State the blood parasite species.
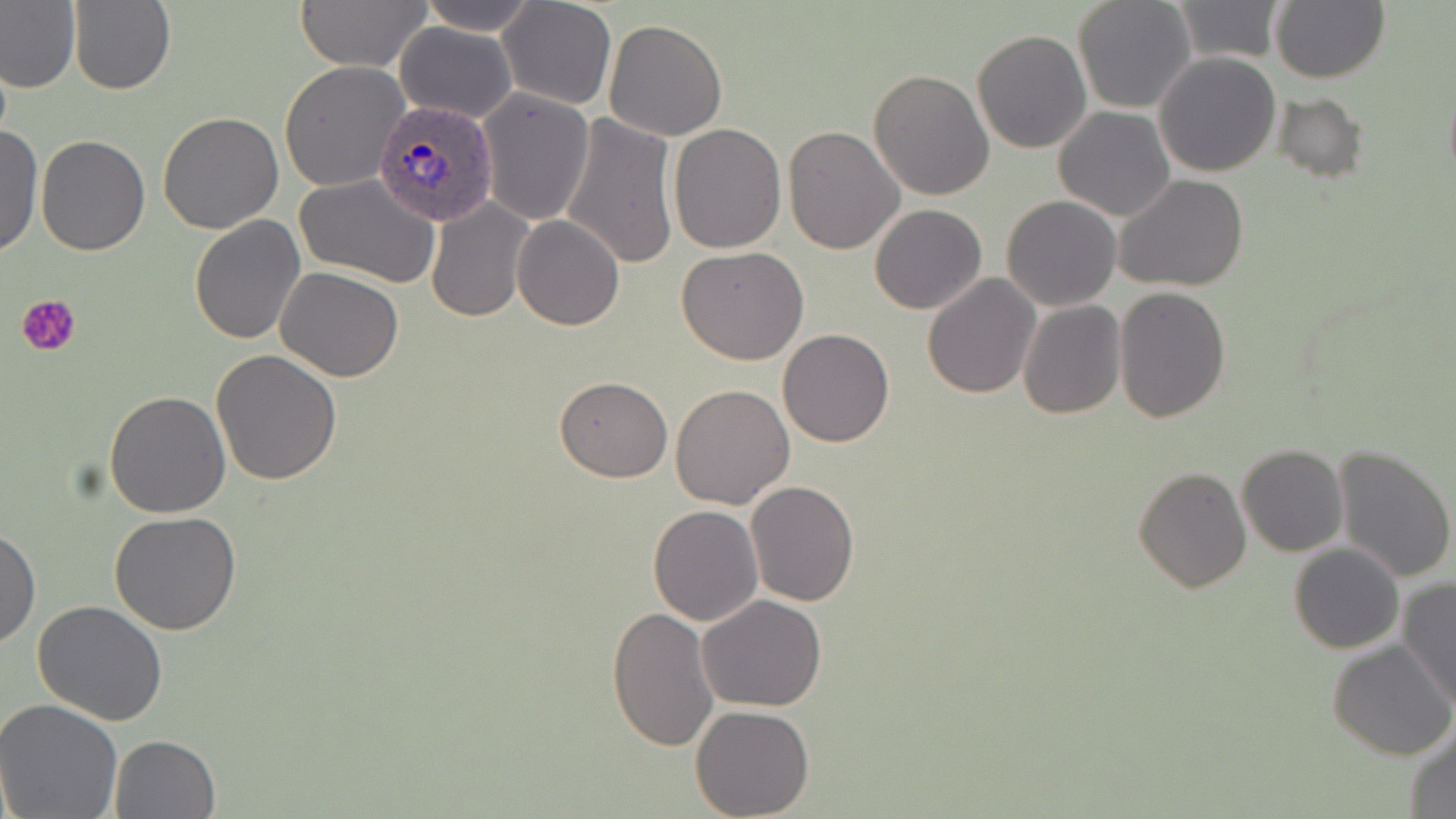
Plasmodium ovale.

Approximate bounding boxes as (x1, y1, x2, y2) in pixels. Uninfected red blood cell locations: (0, 0, 82, 95), (68, 0, 176, 96), (293, 0, 432, 71), (413, 0, 541, 35), (1072, 0, 1196, 115), (1271, 0, 1389, 84), (496, 1, 616, 110), (1171, 1, 1285, 64), (602, 18, 728, 140), (394, 21, 518, 123), (970, 29, 1091, 154), (1154, 51, 1282, 176), (279, 60, 410, 194), (868, 69, 995, 201), (477, 88, 595, 225), (1274, 91, 1367, 182), (1054, 106, 1177, 221), (157, 111, 284, 234), (559, 113, 678, 270), (667, 122, 786, 252), (0, 124, 43, 259), (783, 124, 906, 254), (36, 134, 151, 255), (294, 172, 442, 288), (1114, 173, 1248, 292), (1001, 195, 1122, 312), (426, 199, 533, 321), (868, 204, 988, 314), (189, 215, 306, 343), (512, 215, 625, 330), (678, 245, 809, 366), (276, 266, 405, 383), (922, 272, 1040, 398), (1114, 285, 1231, 423), (1017, 300, 1126, 418), (777, 329, 894, 447), (212, 348, 343, 485), (554, 376, 673, 481), (669, 384, 795, 508), (104, 390, 232, 518), (1236, 444, 1348, 557), (1332, 444, 1456, 583), (1133, 466, 1251, 592), (747, 480, 860, 608), (647, 504, 763, 626), (109, 511, 242, 634), (0, 526, 40, 651), (1289, 543, 1404, 654), (1398, 578, 1455, 709), (697, 595, 827, 712), (32, 599, 168, 725), (606, 604, 720, 751), (1327, 639, 1456, 760), (0, 699, 125, 819), (689, 704, 815, 818), (1404, 723, 1456, 818), (109, 733, 221, 818). Platelet locations: (19, 294, 82, 357). Plasmodium ovale-infected red blood cell locations: (372, 100, 500, 228). One field of a larger specimen. Thin blood film. Light microscopy. May-Grünwald-Giemsa stain. Image is 1456×819 pixels. 1000x magnification.